Describe the morphology of the erythrocytes.
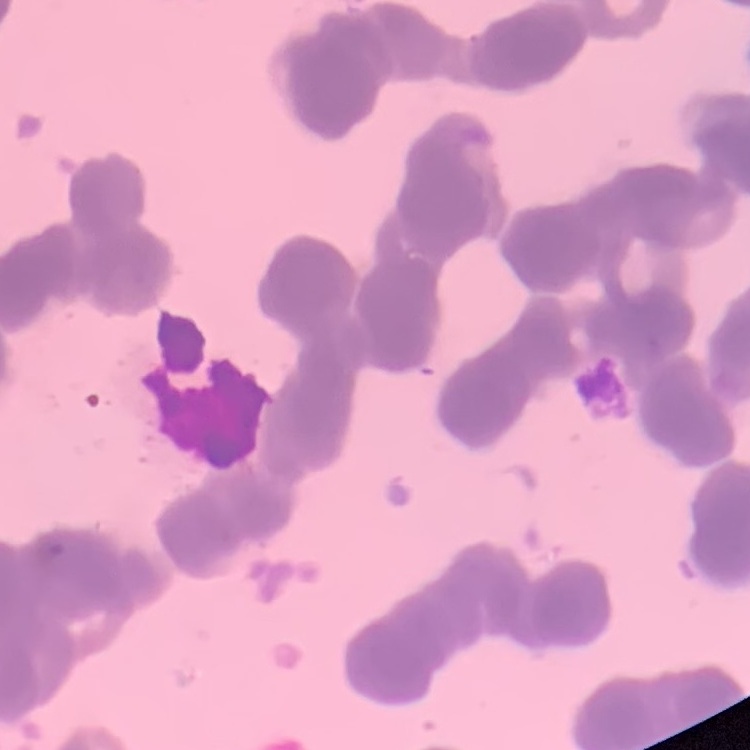
Rouleaux formation.

Stained with either Field's or Giemsa. Thin blood smear. One tile cut from a larger photomicrograph.